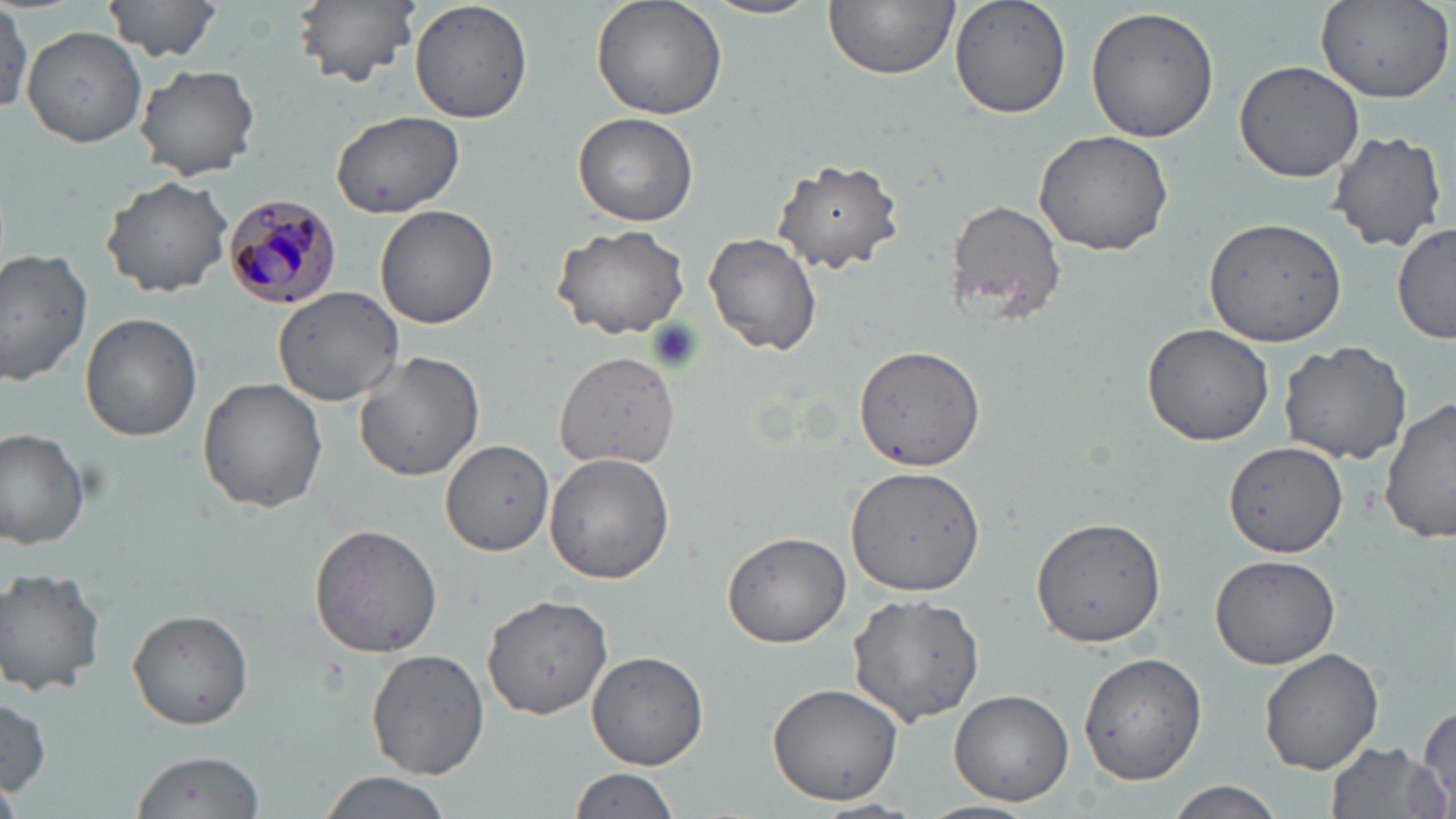

Summary:
  - Coordinate format: approximate bounding boxes as named x1/y1/x2/y2 corners in pixels
  - Plasmodium malariae-infected red blood cell locations: (x1=222, y1=193, x2=342, y2=310)
  - Uninfected red blood cell locations: (x1=101, y1=0, x2=226, y2=61), (x1=291, y1=0, x2=419, y2=88), (x1=408, y1=0, x2=532, y2=123), (x1=591, y1=0, x2=728, y2=121), (x1=698, y1=0, x2=827, y2=19), (x1=823, y1=0, x2=959, y2=78), (x1=949, y1=0, x2=1074, y2=120), (x1=1314, y1=2, x2=1452, y2=104), (x1=0, y1=4, x2=31, y2=114), (x1=1086, y1=6, x2=1224, y2=144), (x1=22, y1=26, x2=147, y2=147), (x1=1234, y1=61, x2=1367, y2=184), (x1=134, y1=64, x2=261, y2=180), (x1=328, y1=108, x2=466, y2=220), (x1=574, y1=111, x2=698, y2=227), (x1=1324, y1=128, x2=1448, y2=254), (x1=1033, y1=129, x2=1174, y2=255), (x1=772, y1=157, x2=904, y2=274), (x1=101, y1=175, x2=234, y2=297), (x1=945, y1=199, x2=1067, y2=323), (x1=376, y1=205, x2=498, y2=330), (x1=1205, y1=216, x2=1349, y2=347), (x1=1392, y1=223, x2=1455, y2=345), (x1=552, y1=224, x2=691, y2=338), (x1=703, y1=231, x2=822, y2=357), (x1=0, y1=245, x2=97, y2=387), (x1=276, y1=287, x2=400, y2=404), (x1=79, y1=313, x2=202, y2=443), (x1=1141, y1=320, x2=1278, y2=447), (x1=1278, y1=339, x2=1415, y2=464), (x1=852, y1=344, x2=987, y2=473), (x1=553, y1=350, x2=680, y2=468), (x1=354, y1=351, x2=484, y2=482), (x1=198, y1=377, x2=328, y2=512), (x1=1382, y1=397, x2=1456, y2=546), (x1=1, y1=428, x2=93, y2=550), (x1=440, y1=438, x2=554, y2=554), (x1=1222, y1=440, x2=1349, y2=558), (x1=544, y1=454, x2=676, y2=585), (x1=845, y1=464, x2=986, y2=595), (x1=1029, y1=516, x2=1167, y2=648), (x1=309, y1=525, x2=443, y2=658), (x1=721, y1=532, x2=850, y2=648), (x1=1210, y1=555, x2=1340, y2=670), (x1=0, y1=566, x2=107, y2=696), (x1=847, y1=588, x2=986, y2=728), (x1=482, y1=593, x2=614, y2=720), (x1=127, y1=611, x2=253, y2=730), (x1=368, y1=647, x2=490, y2=779), (x1=1259, y1=648, x2=1383, y2=773), (x1=587, y1=650, x2=709, y2=770), (x1=1078, y1=651, x2=1207, y2=786), (x1=765, y1=679, x2=906, y2=807), (x1=950, y1=690, x2=1073, y2=804), (x1=1, y1=694, x2=53, y2=798), (x1=1416, y1=702, x2=1454, y2=809), (x1=1325, y1=739, x2=1447, y2=819), (x1=128, y1=749, x2=267, y2=818), (x1=569, y1=766, x2=685, y2=819), (x1=316, y1=772, x2=456, y2=819), (x1=0, y1=780, x2=21, y2=819), (x1=1168, y1=782, x2=1284, y2=818), (x1=916, y1=799, x2=1040, y2=819), (x1=808, y1=800, x2=923, y2=819)
  - Slide-level diagnosis: Plasmodium malariae
  - Magnification: 1000x
  - Modality: light microscopy
  - Field of view: one of a larger specimen
  - Stain: May-Grünwald-Giemsa
  - Preparation: thin blood smear
  - Image size: 1456×819 pixels